Locate and identify every blood parasite.
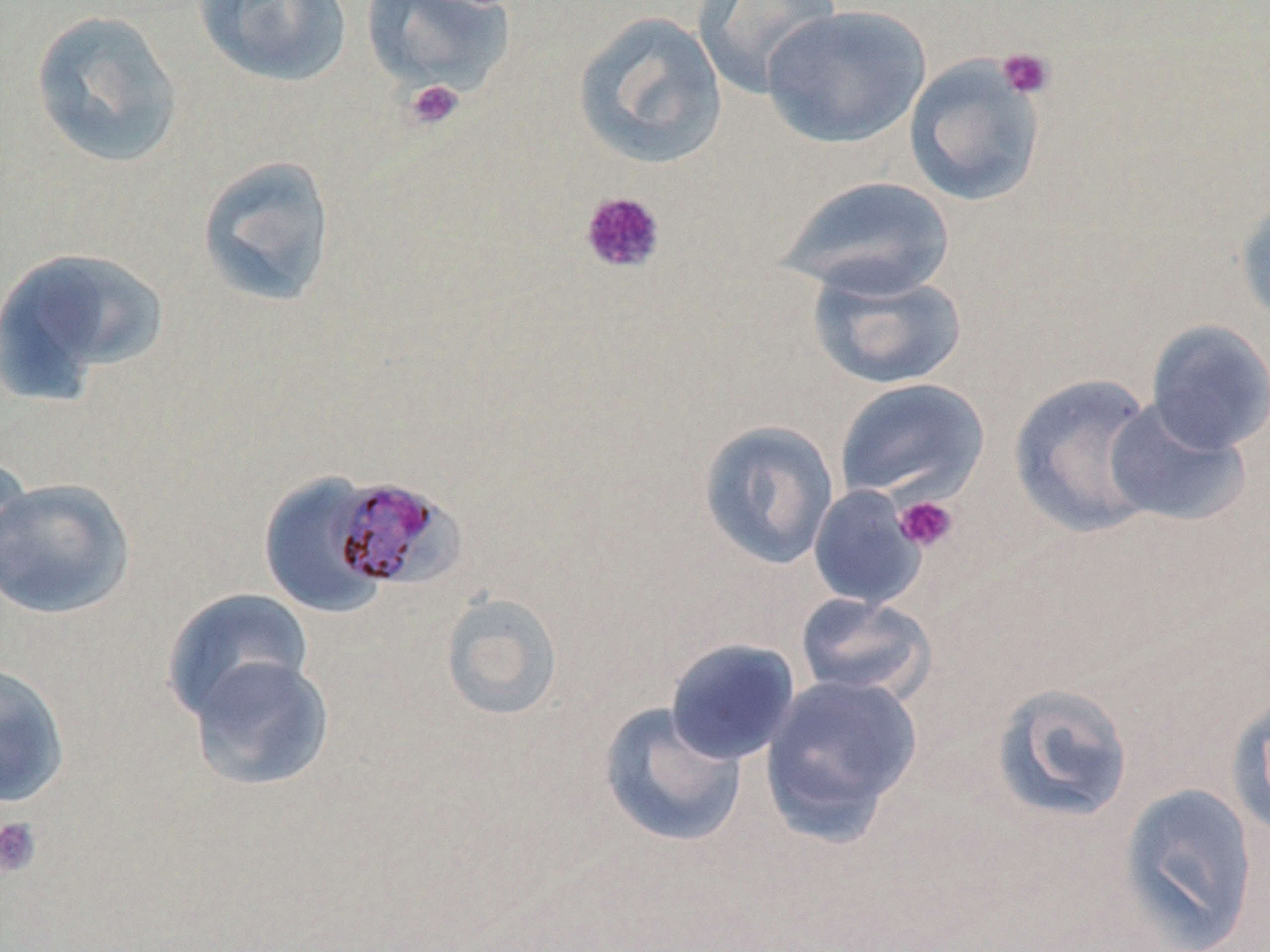

Approximate bounding boxes as (x1, y1, x2, y2) in pixels.
Plasmodium malariae-infected red blood cells: (329, 479, 475, 591).
No Plasmodium falciparum, Plasmodium ovale, Plasmodium vivax, Babesia divergens, or Trypanosoma brucei observed.

Platelet locations: (996, 47, 1056, 100), (404, 78, 465, 132), (578, 190, 667, 275), (894, 495, 959, 553), (0, 816, 43, 878). Uninfected red blood cell locations: (194, 0, 353, 87), (690, 0, 845, 100), (360, 1, 516, 96), (761, 5, 932, 148), (28, 8, 185, 171), (572, 10, 728, 170), (904, 55, 1048, 208), (196, 154, 337, 309), (776, 175, 956, 300), (1234, 186, 1270, 328), (0, 247, 168, 401), (807, 263, 969, 391), (1145, 320, 1270, 454), (1009, 371, 1167, 538), (834, 377, 990, 504), (1103, 398, 1252, 529), (697, 419, 840, 571), (0, 451, 35, 590), (258, 472, 389, 618), (0, 476, 135, 620), (807, 485, 929, 610), (162, 586, 315, 724), (437, 591, 564, 722), (793, 592, 937, 704), (664, 638, 800, 765), (185, 654, 335, 792), (0, 660, 70, 809), (758, 673, 924, 842), (988, 681, 1136, 826), (1230, 691, 1270, 843), (597, 701, 748, 848), (1115, 781, 1262, 950). Slide-level diagnosis: Plasmodium malariae. Image is 1270×952 pixels. Thin blood smear. 1000x magnification. Single field of view. Light microscopy. May-Grünwald-Giemsa stain.